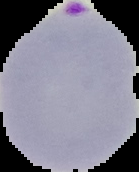
Summary:
  - Result: malaria parasites detected
  - Image type: segmented cell region on a black background
  - Image size: 139×172 pixels
  - Preparation: thin blood film